Point out each Plasmodium parasite.
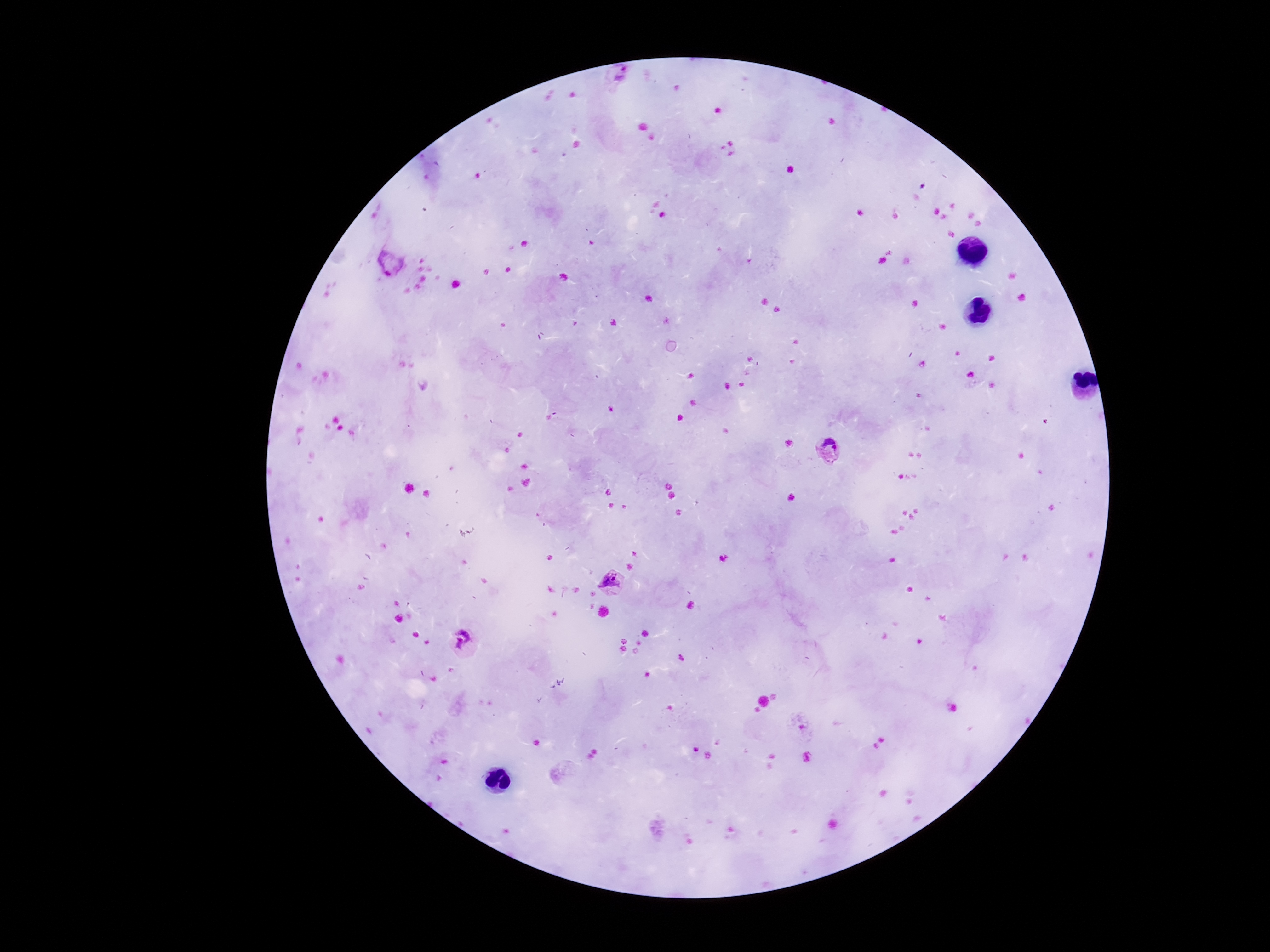
Approximate object centers, in pixels from the top-left corner.
Plasmodium parasites: (x=619, y=79), (x=392, y=263), (x=827, y=450), (x=612, y=584), (x=461, y=643).

Summary:
  - Image size: 1270×952 pixels
  - Magnification: 100x
  - Patient malaria status: infected
  - Capture: smartphone camera through the microscope eyepiece
  - Field of view: one from this slide
  - Stain: Giemsa
  - Preparation: thick blood smear